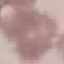

malaria status = uninfected
preparation = thin blood smear
image type = cell patch, automatically extracted from a larger field of view and resized to 64 × 64 pixels
capture = smartphone camera at the microscope eyepiece
stain = Giemsa